State which parasite is depicted.
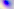

This is Toxoplasma gondii.

Summary:
  - Modality: micrograph
  - Magnification: 400x